Point out every Plasmodium parasite and every leukocyte.
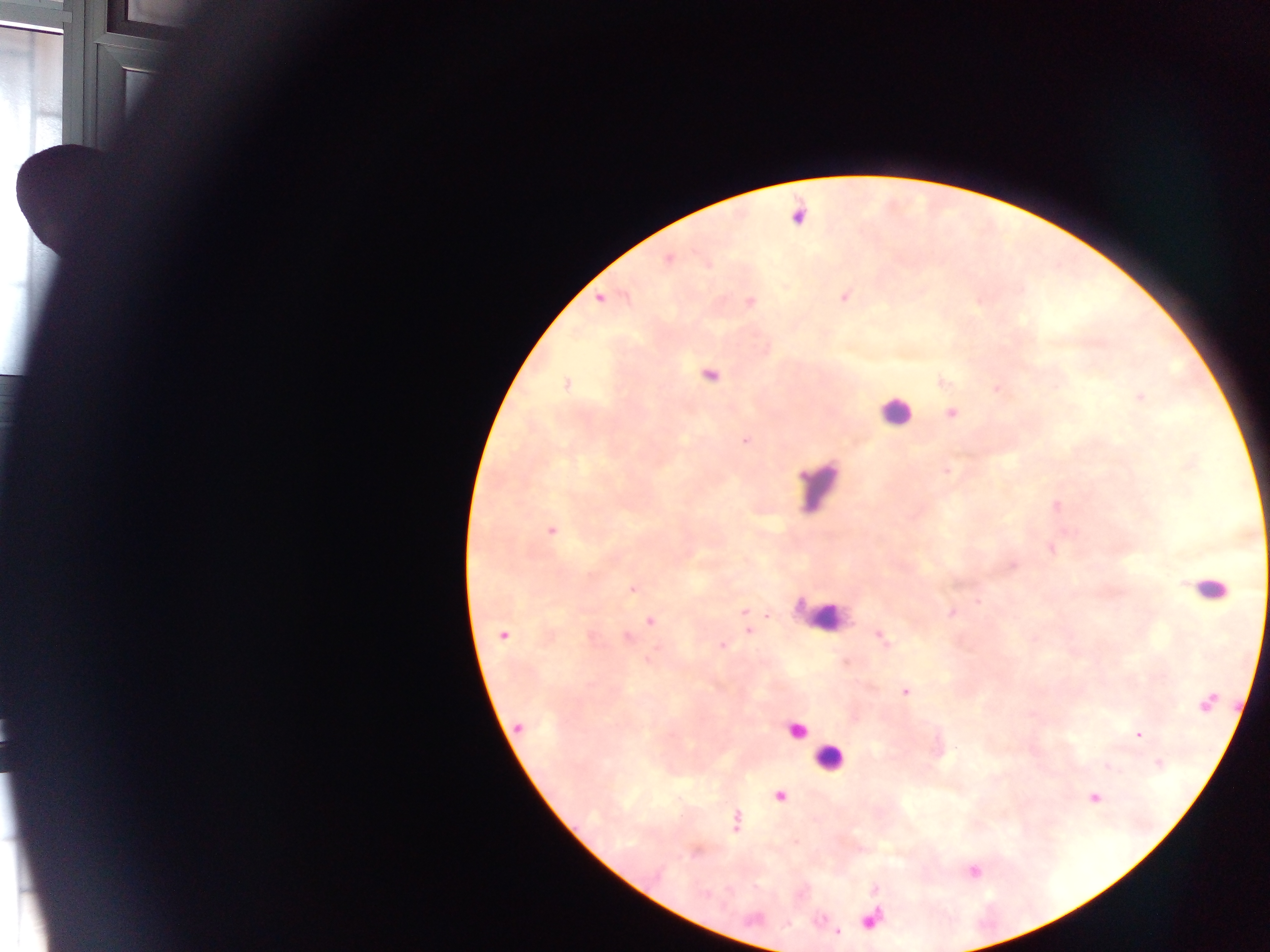

Approximate centers as [x, y] in pixels.
Plasmodium parasites: [669, 259], [845, 297], [600, 300], [750, 301], [711, 375], [566, 384], [1139, 397], [952, 413], [745, 441], [947, 470], [551, 530], [633, 588], [978, 602], [743, 611], [951, 613], [650, 621], [749, 631], [503, 636], [881, 637], [627, 638], [722, 645], [649, 658], [906, 692], [1207, 703], [518, 727], [1139, 735], [1158, 764], [780, 797], [1094, 798], [736, 820].
Leukocytes (some below the resolvable threshold): [894, 411], [818, 487], [1208, 588], [822, 612], [796, 731], [829, 758].

Summary:
  - Field of view: single
  - Preparation: thick blood smear
  - Capture: mobile-phone photograph through a microscope
  - Country: Ghana
  - Image size: 1270×952 pixels